Locate and identify every blood parasite.
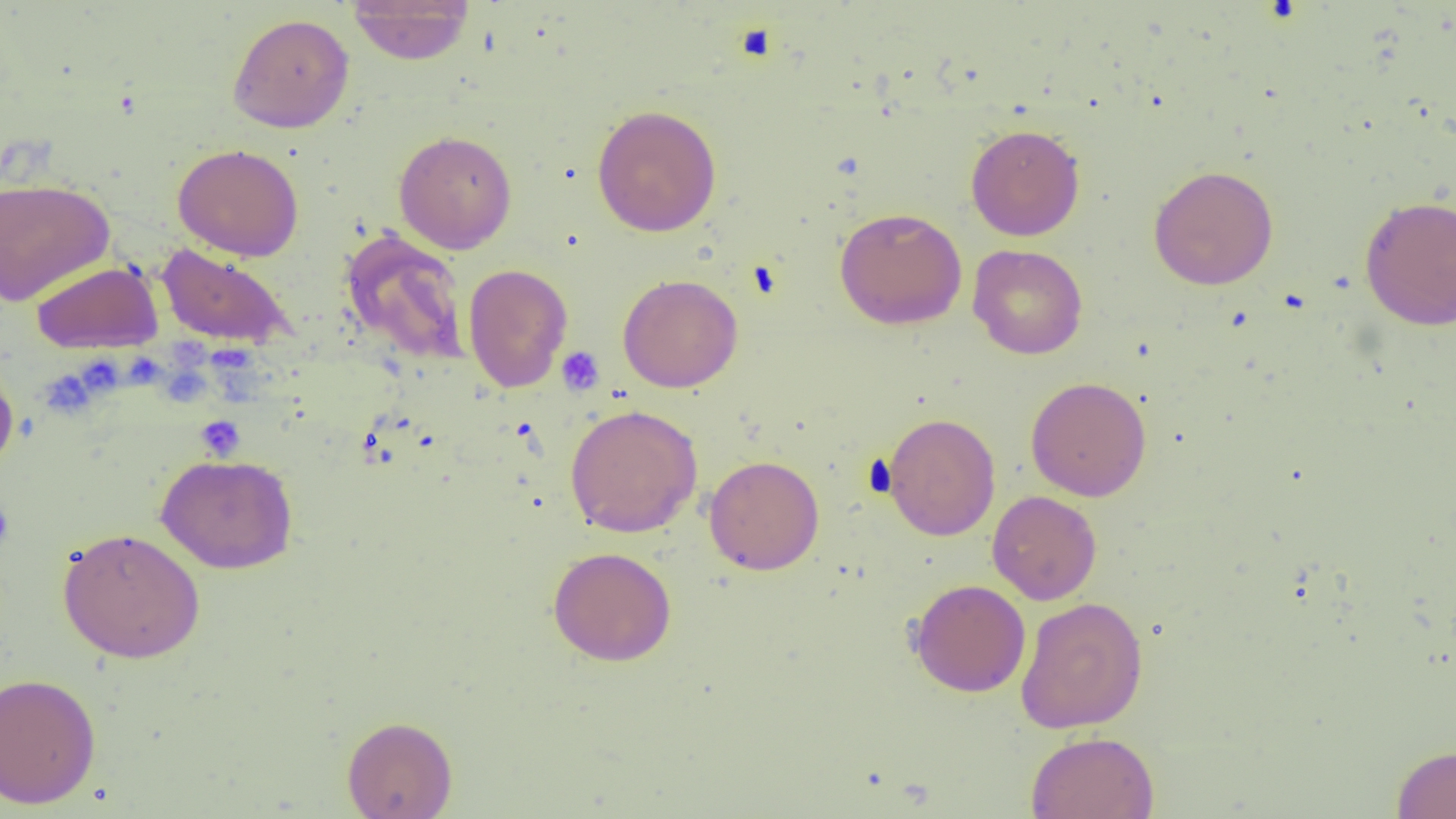

No blood parasites observed.

{
  "slide_level_diagnosis": "no evidence of blood parasites",
  "platelet_locations": "approximate bounding boxes as named x1/y1/x2/y2 corners in pixels: (x1=733, y1=22, x2=779, y2=63), (x1=556, y1=347, x2=604, y2=396), (x1=39, y1=369, x2=97, y2=417), (x1=195, y1=415, x2=245, y2=461), (x1=0, y1=499, x2=14, y2=550)",
  "modality": "optical microscopy",
  "image_size": "1456×819 pixels",
  "preparation": "thin blood film",
  "field_of_view": "single",
  "uninfected_red_blood_cell_locations": "approximate bounding boxes as named x1/y1/x2/y2 corners in pixels: (x1=347, y1=0, x2=474, y2=65), (x1=227, y1=13, x2=355, y2=133), (x1=592, y1=104, x2=722, y2=237), (x1=966, y1=124, x2=1085, y2=241), (x1=394, y1=130, x2=518, y2=253), (x1=173, y1=143, x2=304, y2=261), (x1=1149, y1=165, x2=1278, y2=290), (x1=0, y1=178, x2=113, y2=305), (x1=1359, y1=195, x2=1456, y2=330), (x1=834, y1=207, x2=967, y2=330), (x1=340, y1=229, x2=471, y2=367), (x1=156, y1=244, x2=294, y2=348), (x1=967, y1=244, x2=1088, y2=359), (x1=31, y1=262, x2=162, y2=353), (x1=463, y1=263, x2=573, y2=393), (x1=618, y1=274, x2=743, y2=393), (x1=0, y1=360, x2=19, y2=475), (x1=1025, y1=377, x2=1151, y2=501), (x1=564, y1=404, x2=703, y2=538), (x1=883, y1=412, x2=1001, y2=541), (x1=156, y1=453, x2=298, y2=574), (x1=704, y1=455, x2=824, y2=575), (x1=987, y1=490, x2=1102, y2=605), (x1=57, y1=527, x2=206, y2=664), (x1=548, y1=546, x2=677, y2=666), (x1=908, y1=578, x2=1031, y2=697), (x1=1015, y1=596, x2=1148, y2=733), (x1=0, y1=672, x2=101, y2=809), (x1=342, y1=715, x2=458, y2=819), (x1=1025, y1=731, x2=1159, y2=819), (x1=1391, y1=744, x2=1456, y2=819)",
  "magnification": "1000x"
}